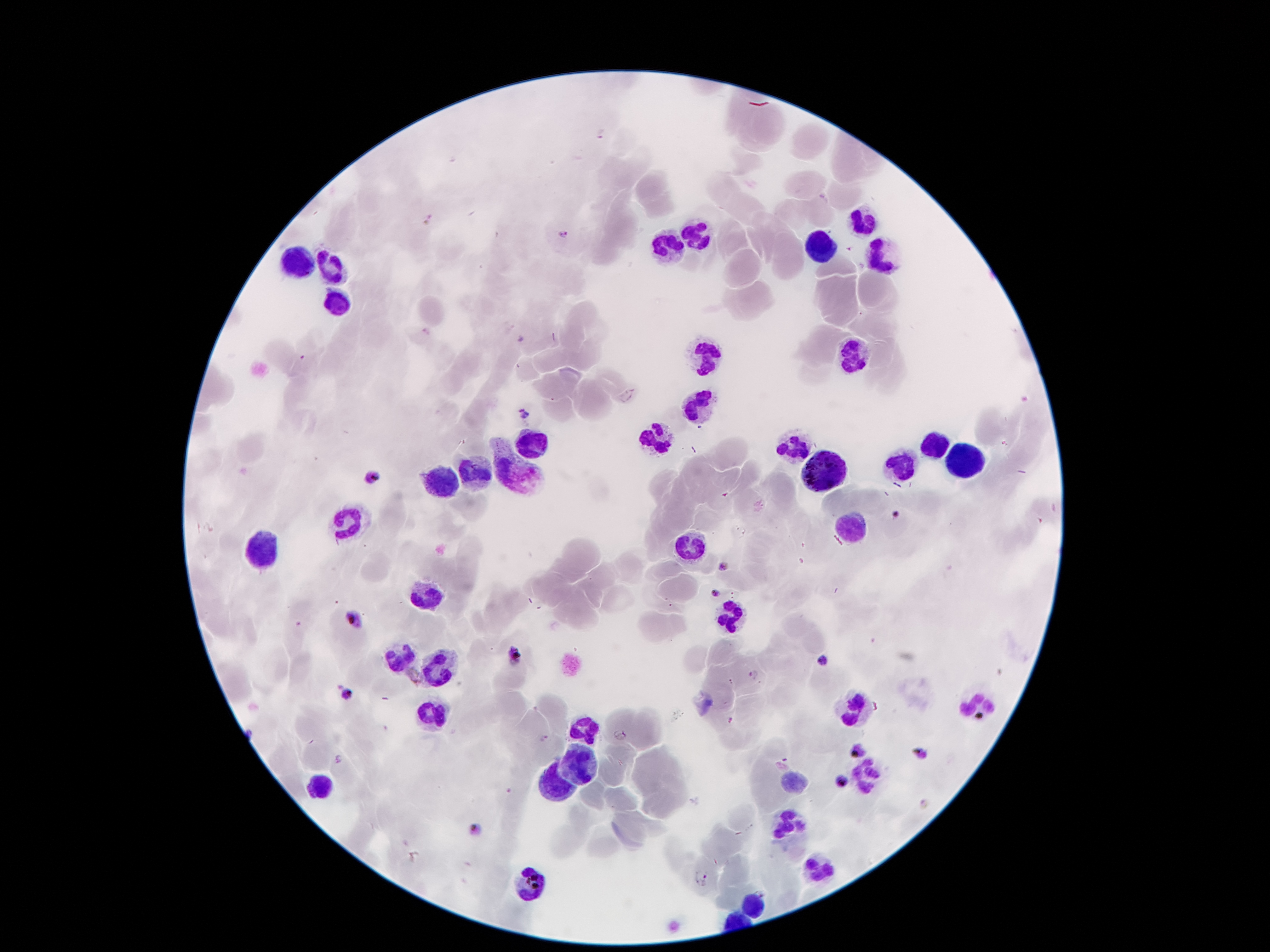

Approximate centers as (x, y) in pixels.
Summary:
  - Leukocyte locations: (863, 221), (696, 239), (824, 248), (665, 254), (879, 254), (293, 261), (329, 268), (337, 298), (711, 356), (852, 358), (700, 403), (660, 433), (532, 442), (789, 442), (936, 447), (957, 462), (899, 465), (516, 467), (822, 471), (475, 475), (446, 484), (848, 522), (346, 524), (693, 544), (260, 557), (424, 595), (731, 617), (401, 661), (435, 666), (978, 705), (852, 710), (433, 712), (583, 730), (579, 763), (864, 776), (793, 779), (324, 785), (556, 785), (789, 829), (821, 867), (527, 883), (753, 903)
  - Plasmodium parasite locations: (565, 234), (523, 413), (372, 476), (896, 515), (723, 567), (713, 592), (356, 618), (515, 657), (824, 661), (754, 674), (346, 693), (620, 735), (543, 738), (858, 751), (919, 753), (339, 759), (841, 781), (475, 828), (703, 878)
  - Magnification: 100x
  - Stain: Giemsa
  - Image size: 1270×952 pixels
  - Preparation: thick peripheral-blood smear
  - Capture: smartphone through the microscope eyepiece
  - Field of view: one from this slide
  - Patient malaria status: infected with Plasmodium falciparum